Report the malaria status.
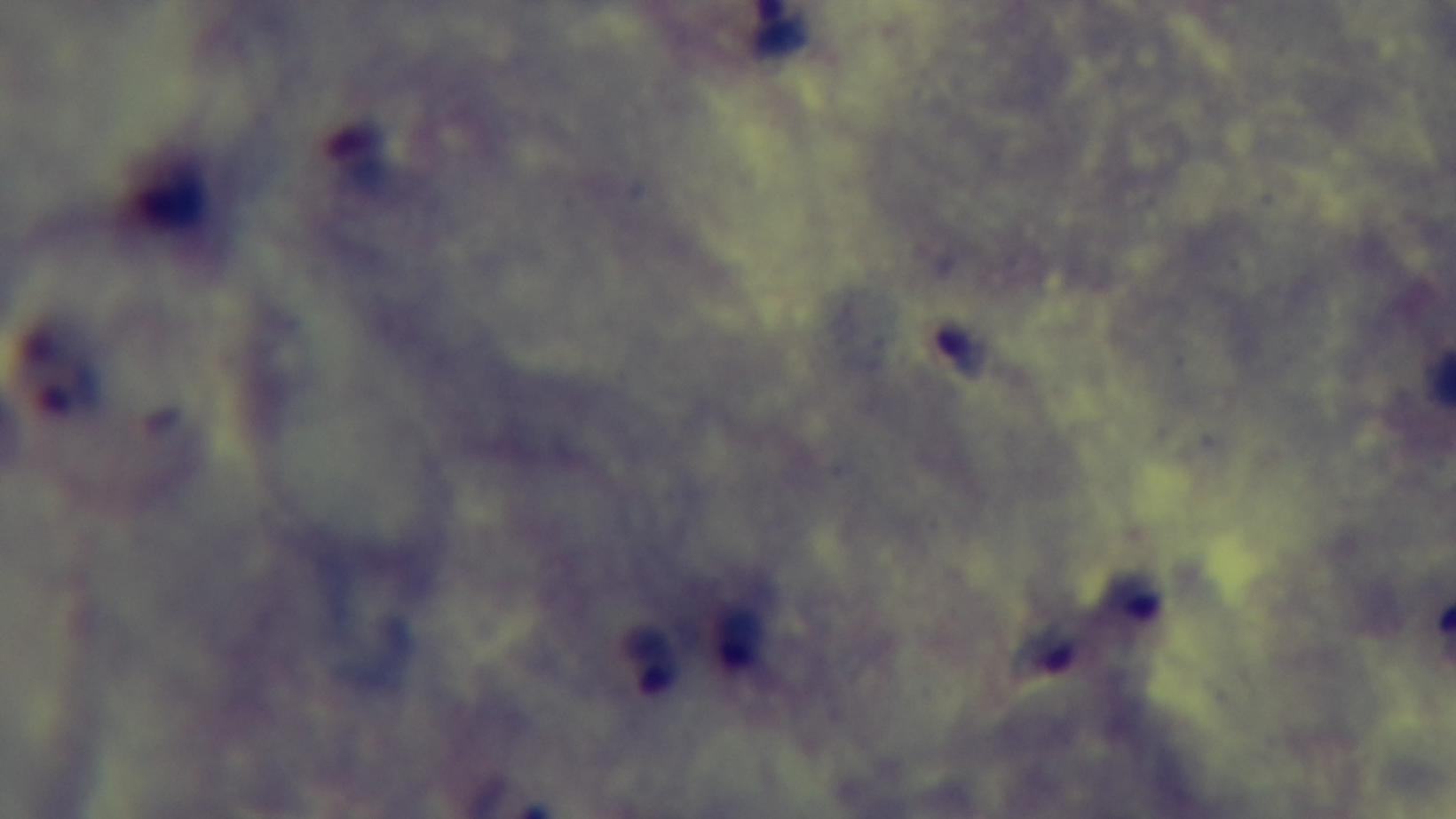

Positive.

{
  "preparation": "thick smear",
  "objective": "100x oil immersion",
  "field_of_view": "one from the slide",
  "modality": "light microscopy",
  "stain": "Giemsa",
  "capture": "mounted 4K digital camera"
}